Point out each leukocyte.
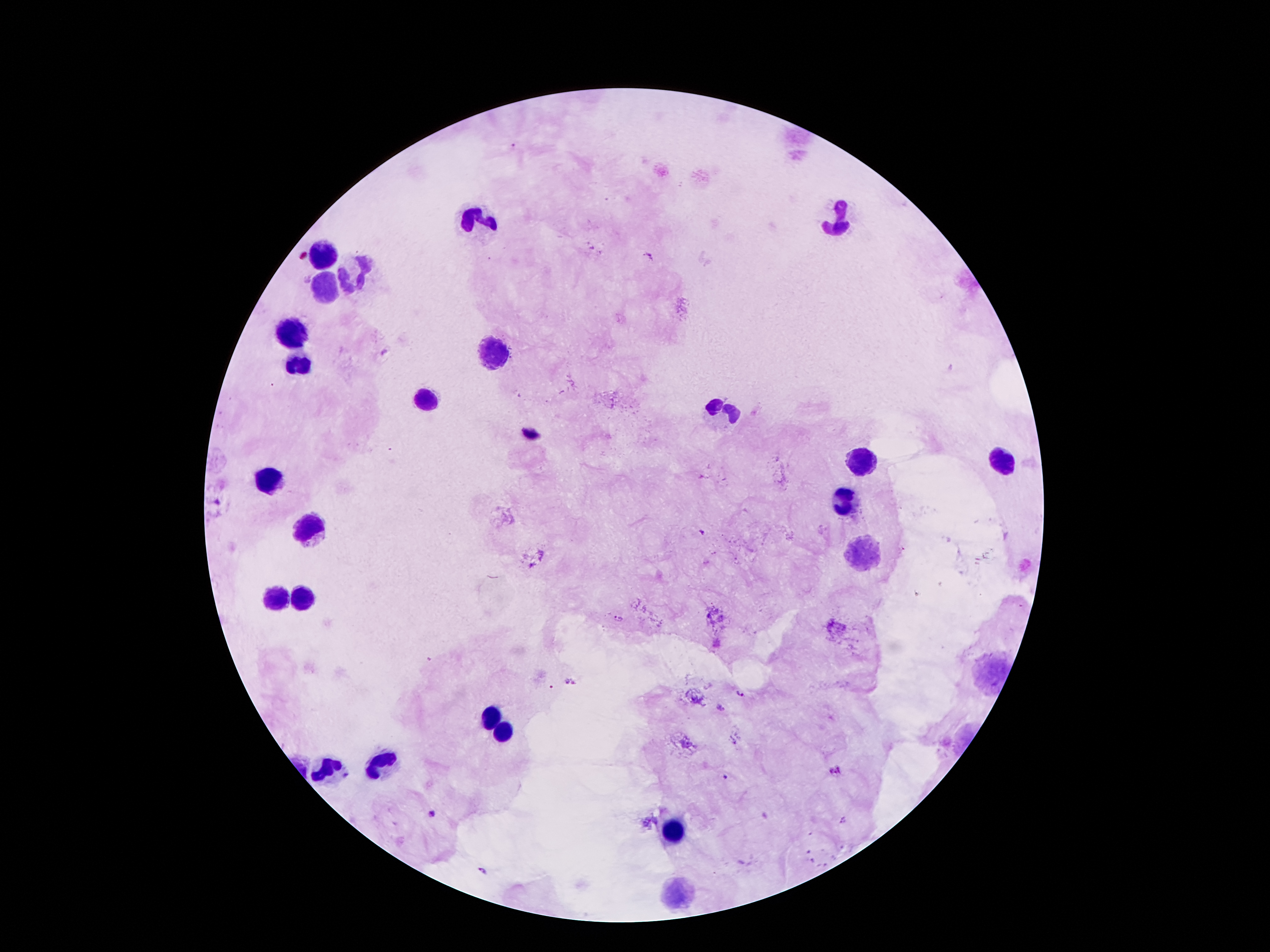

Approximate object centers, in pixels from the top-left corner.
Leukocytes: (x=479, y=218), (x=840, y=220), (x=319, y=253), (x=357, y=270), (x=326, y=283), (x=294, y=337), (x=491, y=350), (x=300, y=362), (x=426, y=400), (x=722, y=411), (x=861, y=461), (x=1002, y=461), (x=265, y=480), (x=851, y=499), (x=309, y=528), (x=861, y=558), (x=279, y=598), (x=305, y=598), (x=489, y=715), (x=502, y=732), (x=380, y=765), (x=330, y=770), (x=676, y=831), (x=676, y=893).

Plasmodium parasite locations: (x=649, y=254), (x=385, y=353), (x=703, y=533), (x=620, y=618), (x=565, y=681), (x=575, y=682), (x=740, y=691), (x=720, y=708), (x=835, y=771), (x=726, y=778), (x=432, y=815), (x=843, y=820), (x=484, y=871). Image is 1270×952 pixels. Thick blood smear. Photographed through the microscope eyepiece with a smartphone camera. Giemsa-stained preparation. Single field of view. Patient malaria status: infected with Plasmodium falciparum. 100x magnification.